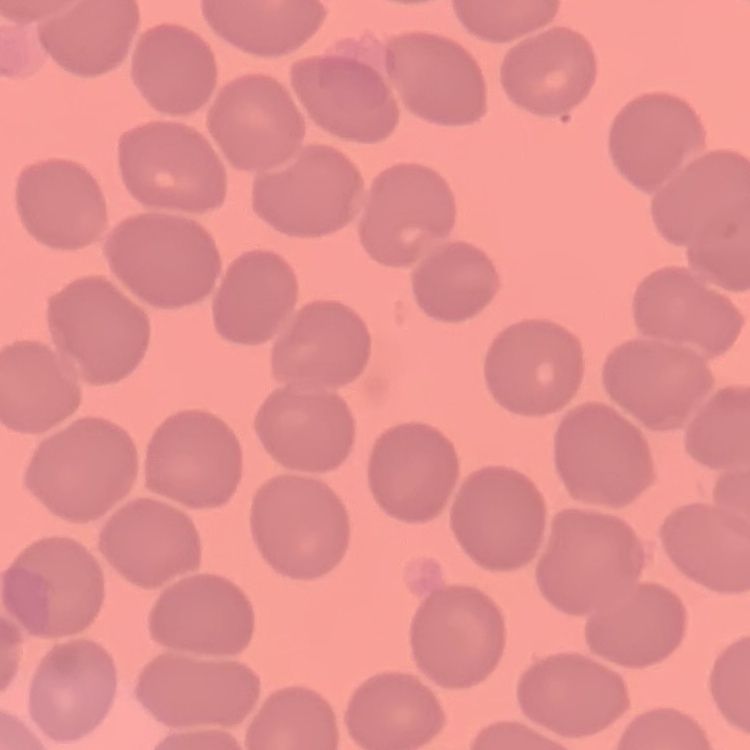

red blood cell morphology = no rouleaux formation
stain = Field's or Giemsa
image type = square crop of a larger photomicrograph
preparation = thin peripheral smear